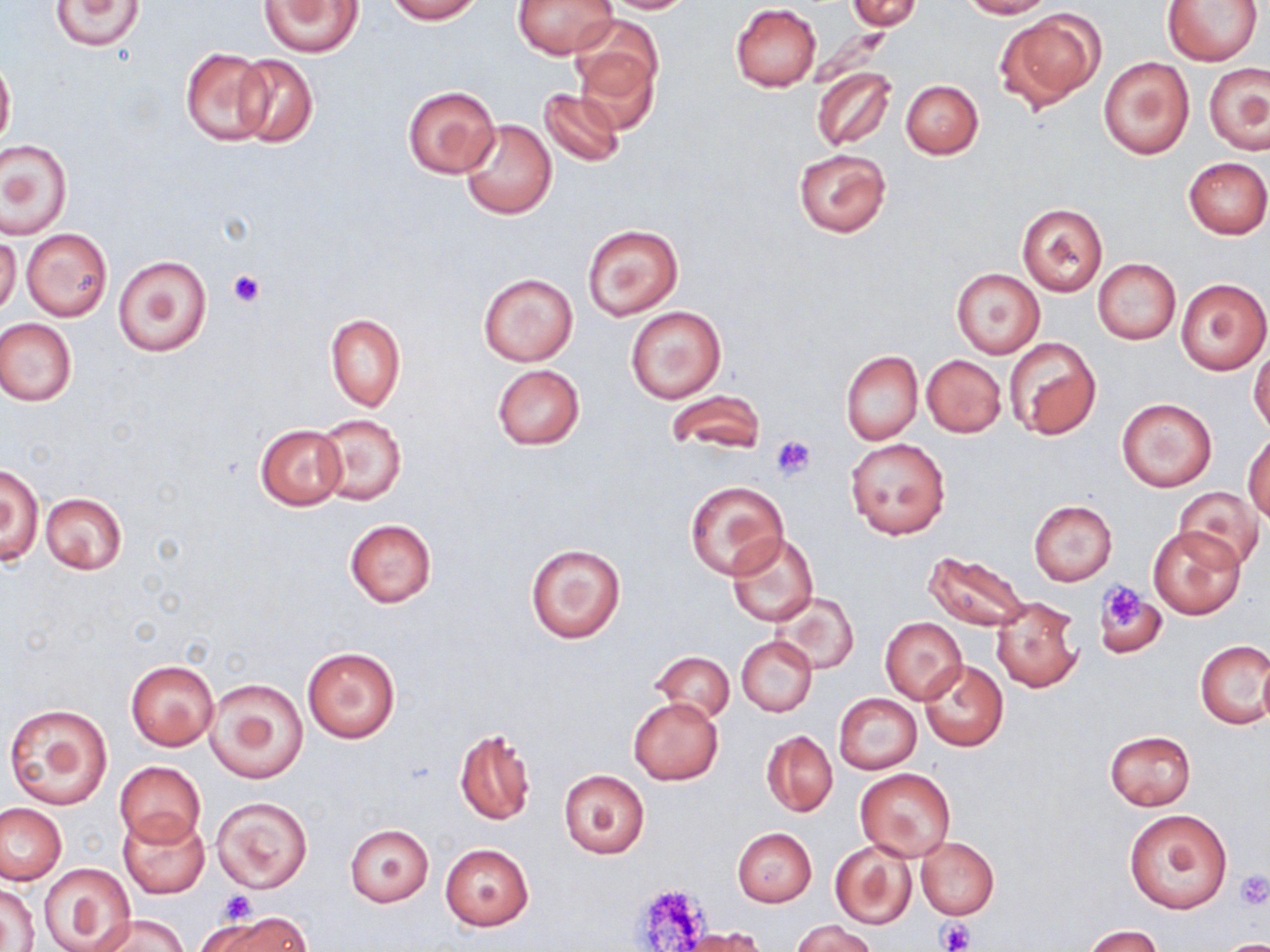
Approximate bounding boxes as (x1, y1, x2, y2) in pixels. Platelet locations: (228, 271, 264, 306), (771, 434, 817, 480), (1096, 579, 1156, 638), (1233, 870, 1270, 910), (629, 886, 710, 950), (216, 889, 260, 925), (938, 921, 974, 952). Uninfected red blood cell locations: (50, 0, 143, 51), (258, 0, 362, 55), (384, 0, 483, 22), (513, 0, 616, 59), (595, 0, 697, 14), (848, 0, 923, 30), (959, 0, 1053, 18), (1162, 0, 1264, 66), (730, 3, 822, 91), (994, 9, 1103, 113), (571, 26, 662, 131), (179, 48, 274, 146), (229, 53, 318, 149), (0, 56, 15, 149), (1098, 56, 1195, 159), (1204, 63, 1269, 155), (810, 66, 895, 152), (899, 79, 984, 159), (402, 84, 501, 179), (538, 87, 627, 167), (459, 117, 556, 220), (1, 139, 71, 238), (793, 149, 890, 236), (1183, 157, 1270, 238), (1017, 204, 1108, 296), (582, 224, 682, 319), (21, 229, 112, 321), (0, 237, 21, 316), (114, 255, 211, 358), (1093, 259, 1181, 344), (951, 269, 1045, 358), (479, 273, 578, 366), (1174, 276, 1270, 376), (625, 304, 727, 404), (325, 314, 405, 411), (0, 318, 78, 407), (1006, 336, 1102, 440), (1249, 348, 1270, 435), (841, 351, 921, 445), (922, 354, 1007, 438), (491, 365, 585, 451), (667, 389, 765, 454), (1116, 398, 1217, 493), (317, 414, 406, 506), (255, 424, 347, 510), (1245, 430, 1270, 521), (844, 437, 950, 539), (1, 464, 44, 567), (685, 481, 786, 579), (1175, 486, 1264, 570), (40, 492, 127, 574), (1029, 501, 1117, 585), (345, 518, 436, 608), (1150, 526, 1246, 620), (725, 532, 819, 628), (524, 542, 627, 644), (924, 550, 1030, 631), (1096, 566, 1183, 650), (770, 592, 858, 674), (991, 596, 1082, 693), (880, 617, 967, 705), (736, 636, 817, 716), (1196, 640, 1270, 730), (301, 647, 401, 742), (651, 651, 735, 722), (126, 659, 218, 750), (919, 659, 1009, 752), (1258, 659, 1270, 730), (205, 677, 309, 784), (834, 693, 922, 774), (628, 696, 723, 785), (3, 703, 113, 809), (454, 728, 536, 825), (1104, 729, 1196, 811), (762, 730, 837, 816), (115, 761, 206, 847), (856, 768, 956, 862), (558, 769, 651, 859), (212, 797, 313, 893), (0, 804, 66, 884), (1124, 808, 1232, 914), (120, 813, 209, 899), (344, 823, 435, 906), (732, 828, 816, 907), (916, 836, 998, 919), (831, 839, 919, 930), (440, 844, 533, 929), (39, 864, 138, 951), (3, 881, 39, 949), (209, 913, 310, 952), (93, 914, 184, 952), (793, 920, 876, 951), (1085, 925, 1162, 952), (680, 928, 770, 952), (1213, 939, 1270, 952). Slide-level diagnosis: no evidence of blood parasites. Captured at 1000x magnification. Thin blood film. May-Grünwald-Giemsa stain. Light microscopy. One field of a larger specimen. Image is 1270×952 pixels.